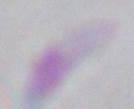
magnification: 1000x
identification: Toxoplasma gondii
modality: photomicrograph